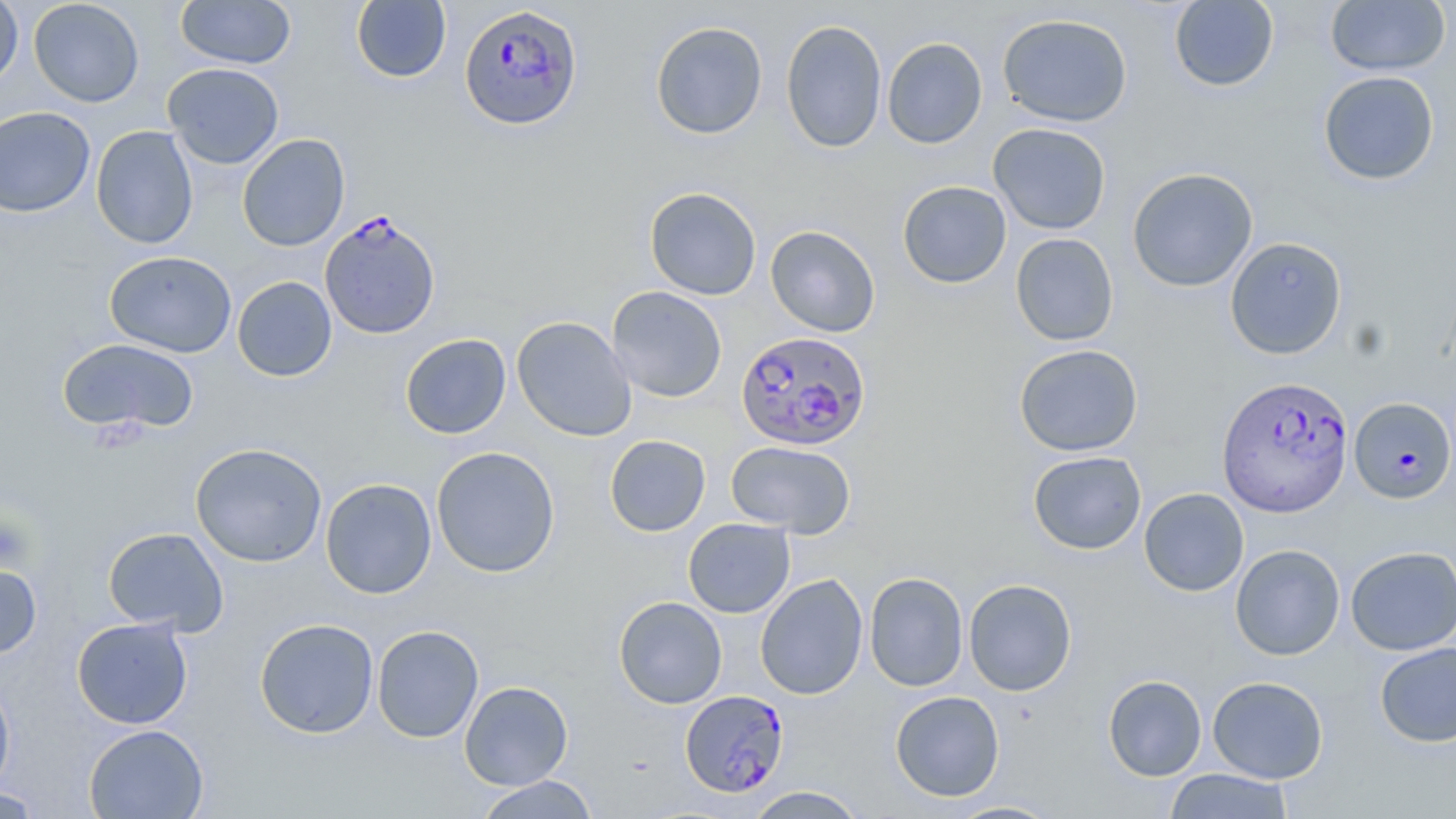
Summary:
  - Coordinate format: approximate bounding boxes as (x1,y1)-(x2,y2) corner pairs in pixels
  - Plasmodium falciparum-infected red blood cell locations: (459,4)-(583,131), (319,211)-(441,340), (736,330)-(871,452), (1217,374)-(1353,517), (1349,397)-(1455,503), (680,690)-(789,797)
  - Uninfected red blood cell locations: (28,0)-(144,107), (0,1)-(23,90), (175,1)-(295,69), (351,1)-(451,83), (1168,1)-(1280,92), (1324,1)-(1451,76), (997,13)-(1133,127), (781,19)-(887,153), (650,21)-(768,140), (882,37)-(987,149), (162,63)-(284,169), (1318,70)-(1440,185), (0,106)-(95,217), (988,123)-(1111,235), (91,125)-(198,249), (236,134)-(350,252), (1127,167)-(1258,291), (897,180)-(1011,288), (645,187)-(761,300), (765,225)-(880,337), (1010,233)-(1119,346), (1225,236)-(1347,359), (104,251)-(237,358), (232,276)-(337,381), (607,286)-(727,402), (512,316)-(636,441), (400,333)-(511,439), (56,338)-(199,435), (1014,343)-(1143,457), (605,435)-(711,537), (725,441)-(856,538), (190,442)-(328,567), (431,446)-(560,578), (1028,450)-(1147,555), (320,478)-(437,599), (1139,487)-(1249,596), (683,518)-(795,618), (102,526)-(229,636), (1230,543)-(1345,660), (1345,545)-(1456,655), (0,562)-(42,659), (864,572)-(968,692), (755,574)-(868,700), (963,578)-(1077,696), (613,596)-(727,708), (71,616)-(193,728), (254,618)-(379,738), (372,625)-(484,743), (1374,642)-(1456,747), (0,675)-(16,799), (1103,675)-(1207,781), (1207,676)-(1328,783), (459,680)-(573,790), (890,690)-(1005,801), (84,724)-(209,819), (1164,768)-(1294,818), (473,775)-(600,818), (1,785)-(47,818), (744,786)-(868,818), (946,800)-(1062,818)
  - Platelet locations: (0,514)-(35,571)
  - Slide-level diagnosis: Plasmodium falciparum
  - Modality: light microscopy
  - Preparation: thin blood film
  - Stain: May-Grünwald-Giemsa
  - Magnification: 1000x
  - Field of view: one of a larger specimen
  - Image size: 1456×819 pixels